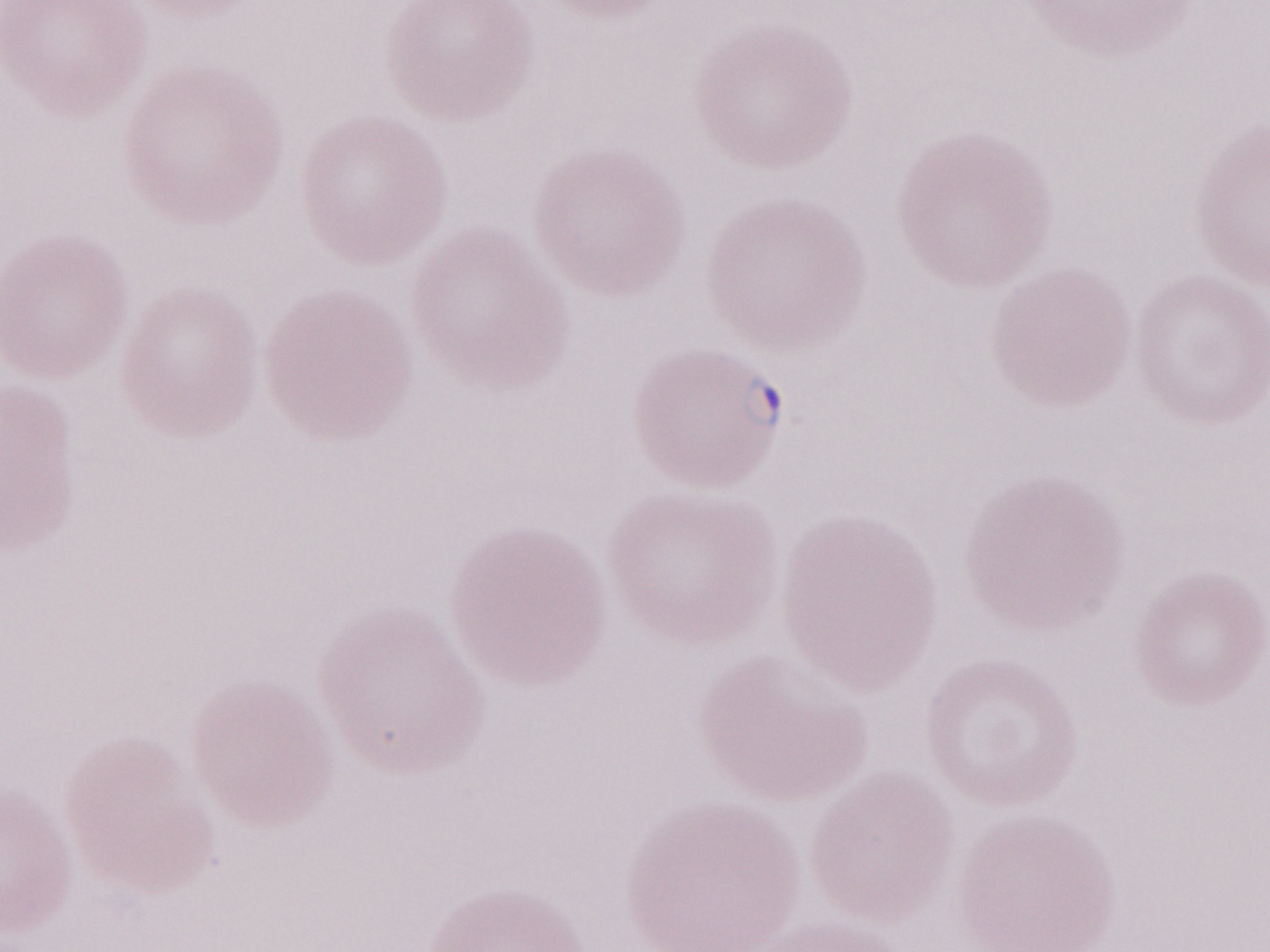
1,000x magnification. One field of this slide. May-Grünwald-Giemsa-stained preparation. Thin blood smear. Patient-level malaria diagnosis: positive. Image is 1270×952 pixels. Olympus BX43 microscope, Olympus DP73 camera.